Describe the morphology of the red blood cells.
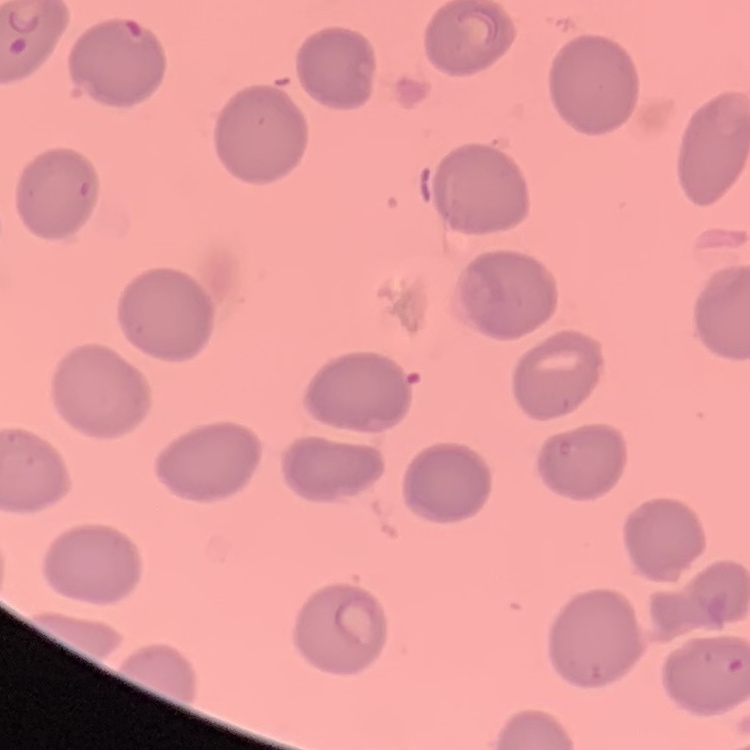

No rouleaux formation.

stain: Field's or Giemsa
preparation: thin blood smear
image_type: one tile cut from a larger photomicrograph